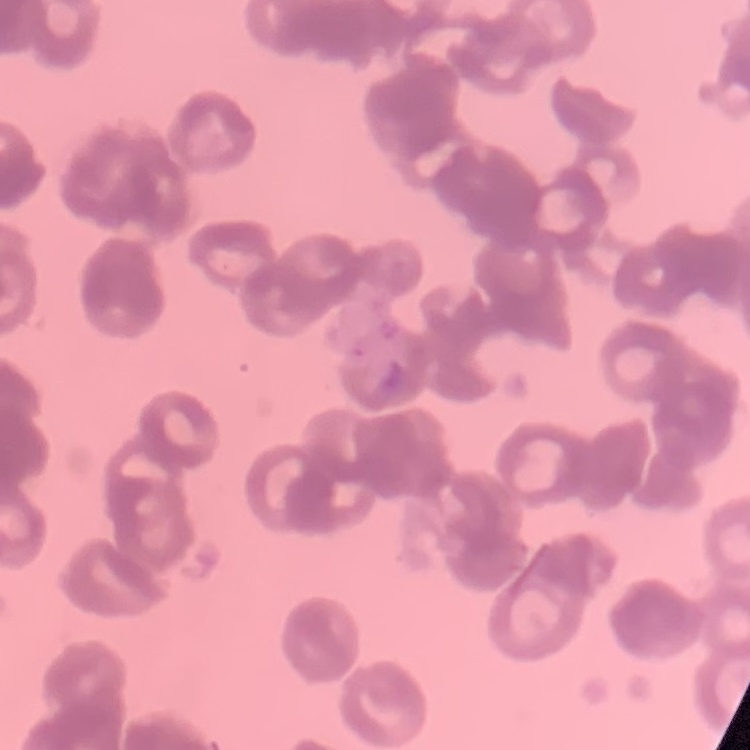
The erythrocytes exhibit rouleaux formation. Square crop of a larger photomicrograph. Stained with either Field's or Giemsa. Thin peripheral smear.